Describe the morphology of the erythrocytes.
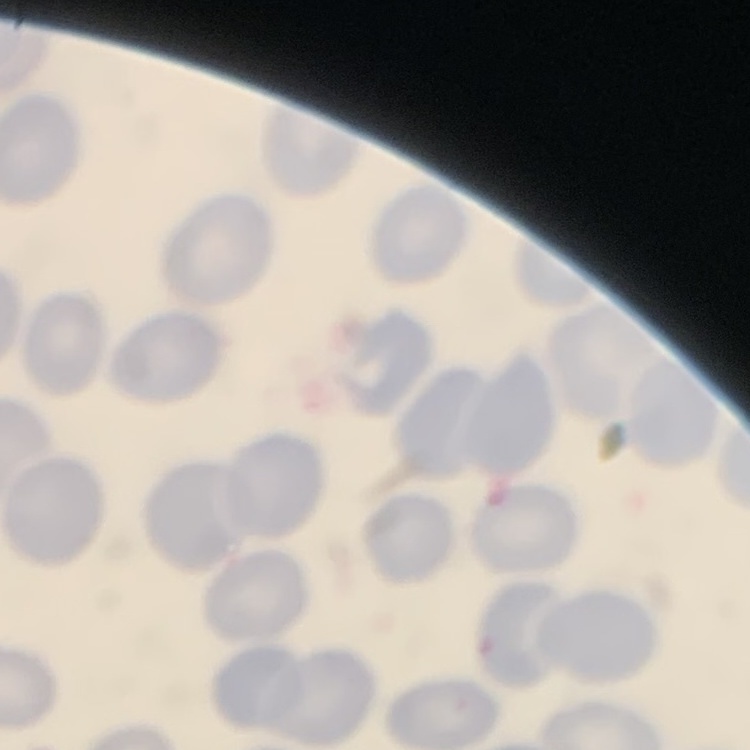
They show no rouleaux formation.

Summary:
  - Image type: square crop of a larger photomicrograph
  - Preparation: thin blood film
  - Stain: Field's or Giemsa